Describe the morphology of the erythrocytes.
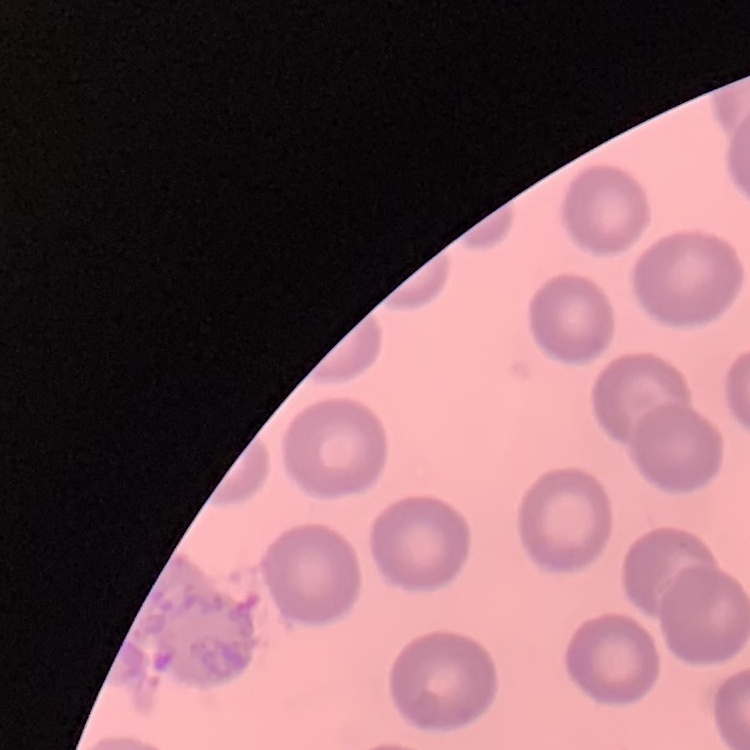
They show no rouleaux formation.

Summary:
  - Preparation: thin peripheral smear
  - Stain: Field's or Giemsa
  - Image type: square crop of a larger photomicrograph